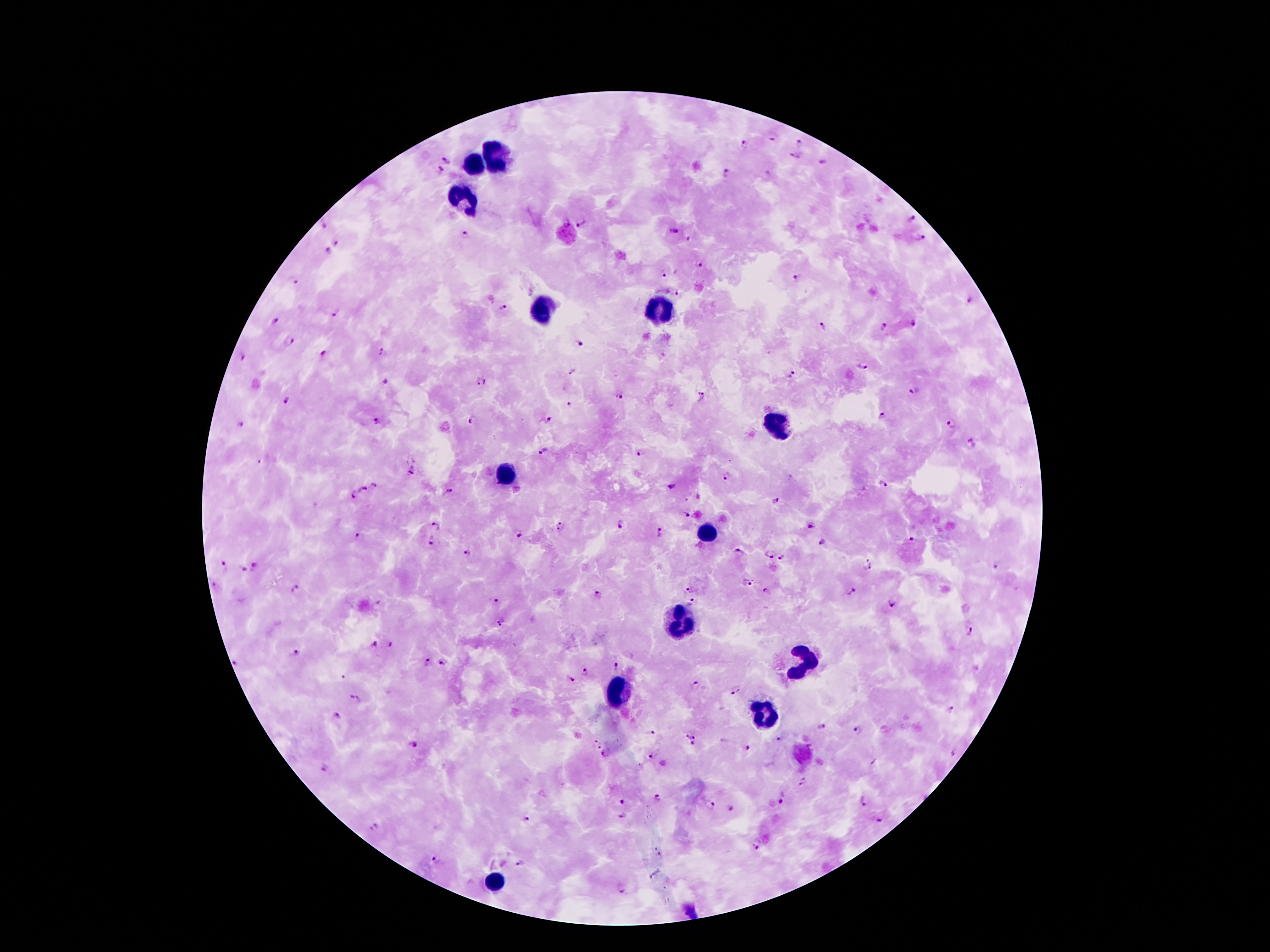
Approximate centers as [x, y] in pixels.
Summary:
  - Leukocyte locations: [497, 154], [474, 163], [462, 199], [544, 311], [658, 313], [774, 426], [506, 474], [708, 529], [681, 622], [799, 661], [619, 688], [767, 714], [492, 879]
  - Malaria parasite locations: [773, 136], [799, 142], [744, 144], [795, 156], [445, 159], [824, 162], [441, 169], [728, 173], [913, 217], [581, 223], [673, 228], [465, 233], [690, 238], [920, 238], [336, 242], [329, 249], [699, 265], [664, 274], [798, 277], [297, 281], [678, 295], [972, 300], [504, 308], [335, 312], [273, 321], [915, 324], [823, 328], [884, 328], [289, 340], [580, 343], [324, 353], [383, 354], [241, 356], [863, 366], [573, 371], [791, 375], [384, 383], [484, 383], [913, 393], [621, 394], [700, 397], [286, 400], [569, 403], [882, 415], [376, 420], [545, 420], [473, 421], [240, 423], [951, 423], [972, 442], [543, 451], [640, 452], [259, 459], [413, 471], [728, 476], [882, 484], [375, 485], [673, 486], [363, 490], [448, 492], [352, 494], [775, 499], [685, 514], [810, 524], [621, 525], [436, 526], [561, 526], [659, 532], [518, 534], [358, 535], [911, 539], [824, 541], [430, 542], [738, 551], [468, 552], [770, 555], [782, 556], [869, 561], [224, 563], [257, 563], [996, 566], [244, 569], [867, 570], [748, 581], [296, 588], [690, 589], [849, 589], [769, 590], [597, 595], [496, 601], [693, 602], [893, 604], [501, 622], [971, 633], [374, 644], [391, 645], [294, 653], [236, 662], [428, 662], [443, 662], [616, 667], [585, 672], [572, 679], [695, 684], [737, 691], [357, 699], [952, 711], [338, 715], [821, 725], [858, 729], [650, 732], [685, 736], [779, 738], [593, 741], [696, 741], [601, 745], [414, 746], [747, 747], [955, 752], [607, 753], [652, 756], [326, 766], [803, 780], [657, 798], [865, 798], [784, 799], [623, 802], [710, 804], [733, 809], [622, 815], [879, 819], [527, 820], [373, 825], [755, 846], [436, 860], [521, 863], [623, 891]
  - Patient malaria status: infected with Plasmodium falciparum
  - Image size: 1270×952 pixels
  - Magnification: 100x
  - Capture: smartphone camera through the microscope eyepiece
  - Stain: Giemsa
  - Field of view: one from this slide
  - Preparation: thick blood smear